Outline each Plasmodium falciparum-infected red blood cell.
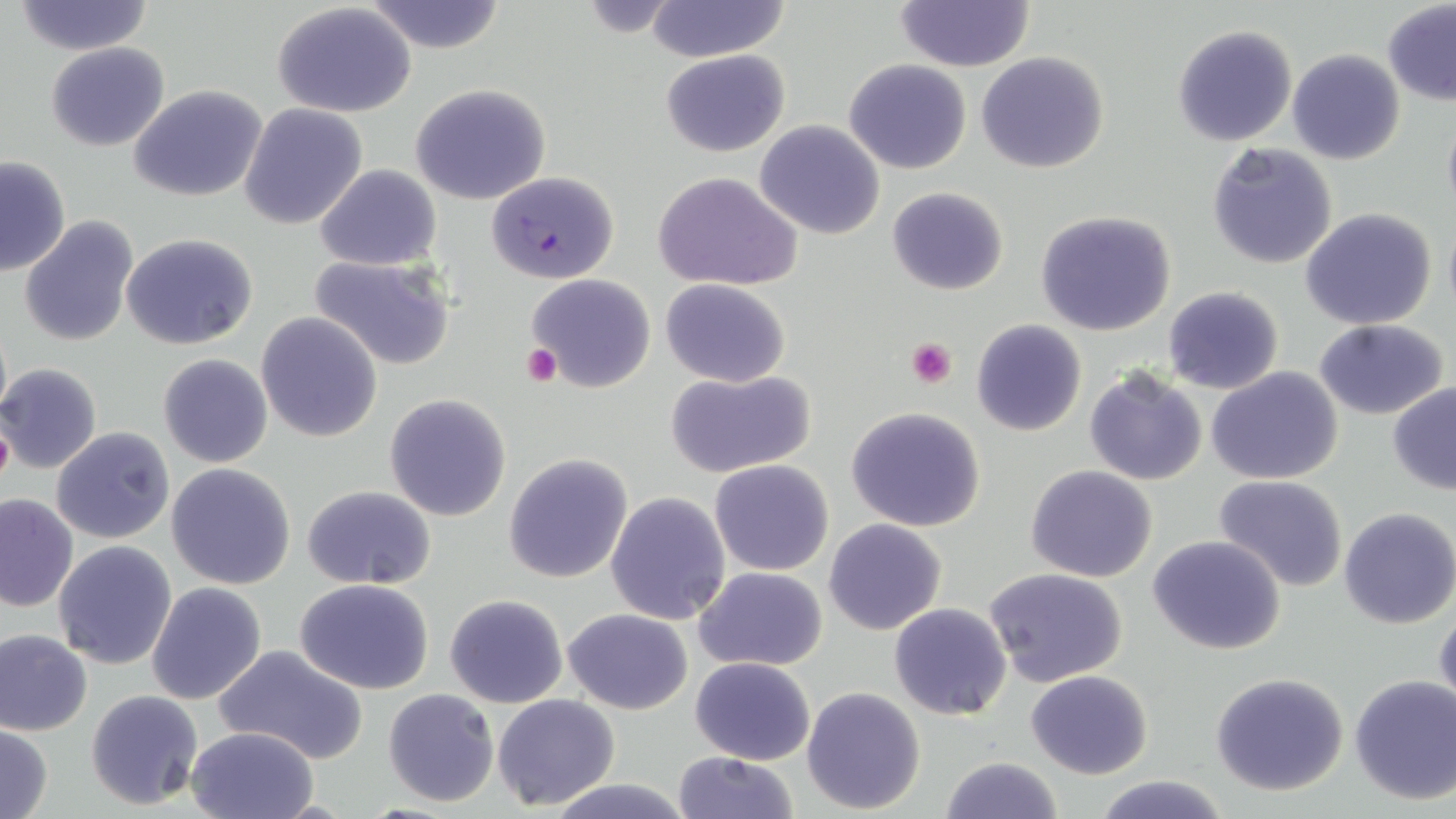

Approximate bounding boxes as [x1, y1, x2, y2] in pixels.
Plasmodium falciparum-infected red blood cells: [487, 170, 619, 283].

Platelet locations: [907, 338, 957, 388], [521, 344, 561, 384], [0, 416, 14, 490]. Uninfected red blood cell locations: [11, 0, 154, 56], [644, 0, 793, 64], [363, 1, 508, 53], [894, 2, 1035, 72], [273, 3, 416, 118], [1382, 3, 1456, 106], [1172, 23, 1298, 148], [45, 41, 170, 151], [660, 49, 791, 158], [1287, 49, 1405, 165], [976, 52, 1109, 174], [843, 58, 972, 175], [409, 83, 551, 205], [130, 86, 267, 202], [239, 103, 367, 229], [1441, 112, 1456, 223], [755, 120, 885, 240], [1207, 143, 1339, 269], [0, 155, 70, 277], [315, 164, 440, 271], [653, 170, 803, 291], [887, 187, 1010, 296], [1300, 207, 1438, 330], [1034, 210, 1177, 336], [19, 216, 139, 346], [121, 232, 259, 350], [307, 254, 454, 372], [525, 273, 656, 393], [659, 277, 792, 387], [1162, 287, 1284, 395], [256, 312, 383, 443], [1313, 318, 1449, 420], [971, 319, 1088, 437], [158, 354, 273, 468], [0, 362, 103, 475], [1085, 365, 1208, 487], [1206, 367, 1343, 485], [665, 368, 815, 479], [1388, 381, 1456, 494], [383, 393, 512, 521], [844, 406, 987, 533], [52, 427, 175, 544], [504, 453, 632, 583], [710, 460, 835, 575], [166, 462, 295, 590], [1026, 465, 1159, 582], [1214, 475, 1350, 591], [303, 486, 437, 589], [605, 491, 732, 626], [0, 492, 78, 612], [1338, 507, 1456, 629], [823, 519, 948, 636], [1147, 534, 1287, 655], [53, 540, 178, 669], [694, 566, 826, 672], [983, 566, 1129, 686], [295, 579, 437, 694], [146, 582, 267, 704], [444, 593, 569, 709], [888, 601, 1013, 721], [1434, 607, 1455, 716], [563, 608, 693, 713], [0, 628, 93, 736], [211, 644, 370, 764], [690, 657, 816, 766], [1025, 669, 1153, 778], [1209, 671, 1351, 795], [1349, 674, 1456, 806], [801, 687, 926, 812], [383, 688, 499, 808], [85, 689, 204, 811], [493, 693, 620, 809], [0, 723, 53, 819], [186, 728, 316, 819], [673, 752, 800, 818], [939, 755, 1063, 819], [1092, 773, 1233, 818], [541, 776, 698, 819]. Slide-level diagnosis: Plasmodium falciparum. Light microscopy. Thin blood film. Image is 1456×819 pixels. One field of a larger specimen. May-Grünwald-Giemsa stain. Captured at 1000x magnification.